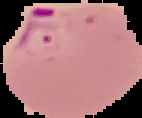
Summary:
  - Result: malaria parasites detected
  - Preparation: thin blood smear
  - Image size: 142×118 pixels
  - Image type: segmented cell region on a black background